Locate every uninfected red blood cell.
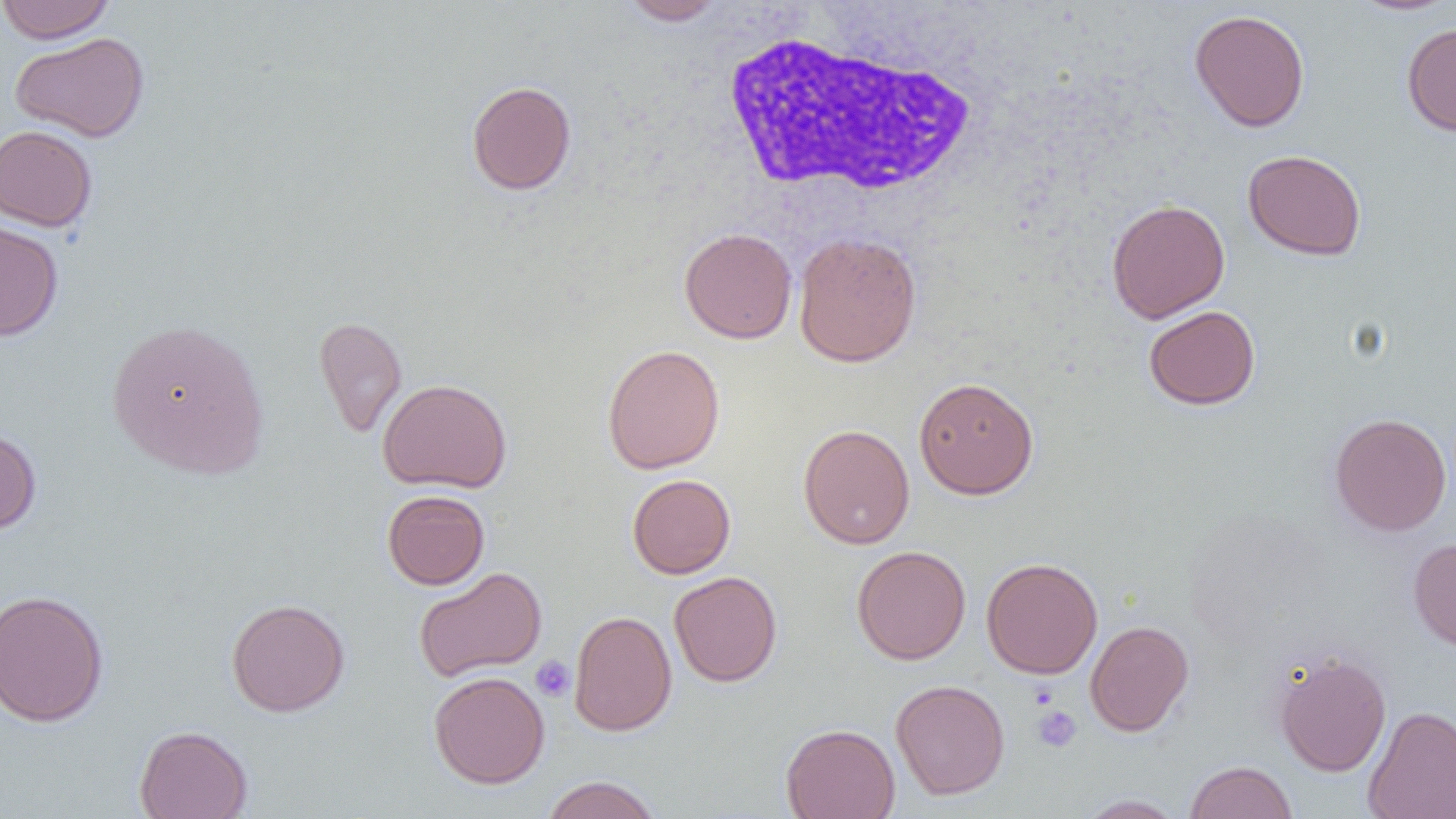

Approximate bounding boxes as [x1, y1, x2, y2] in pixels.
Uninfected red blood cells: [0, 0, 116, 43], [618, 0, 727, 26], [1349, 1, 1456, 16], [1189, 9, 1310, 132], [1402, 23, 1456, 136], [10, 32, 149, 143], [466, 80, 577, 195], [0, 125, 98, 232], [1242, 149, 1367, 261], [1106, 198, 1230, 323], [0, 217, 63, 342], [679, 227, 797, 344], [793, 232, 922, 367], [1143, 305, 1260, 410], [313, 315, 407, 438], [106, 318, 270, 480], [602, 344, 725, 474], [913, 376, 1039, 499], [377, 378, 512, 494], [1330, 412, 1452, 537], [0, 423, 41, 535], [798, 424, 914, 549], [627, 474, 736, 578], [382, 490, 490, 589], [1408, 536, 1456, 652], [852, 545, 971, 665], [981, 557, 1102, 678], [413, 567, 547, 683], [669, 570, 782, 687], [0, 589, 109, 728], [226, 598, 350, 716], [568, 610, 678, 735], [1085, 620, 1194, 736], [1273, 651, 1391, 777], [428, 671, 549, 788], [890, 679, 1009, 800], [1362, 705, 1456, 819], [780, 723, 900, 819], [134, 725, 252, 819], [1184, 760, 1298, 819], [541, 775, 662, 819], [1074, 794, 1187, 818].

slide-level diagnosis = negative for blood parasites
platelet locations = approximate bounding boxes as [x1, y1, x2, y2] in pixels: [531, 656, 576, 702], [1030, 682, 1060, 710], [1030, 705, 1082, 752]
modality = light microscopy
preparation = thin blood smear
image size = 1456×819 pixels
magnification = 1000x
white blood cell locations = approximate bounding boxes as [x1, y1, x2, y2] in pixels: [715, 26, 987, 200]
field of view = single